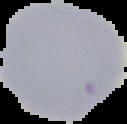
{
  "image_size": "127×124 pixels",
  "image_type": "segmented cell region with the area outside set to black",
  "result": "no malaria parasites detected",
  "preparation": "thin blood smear"
}